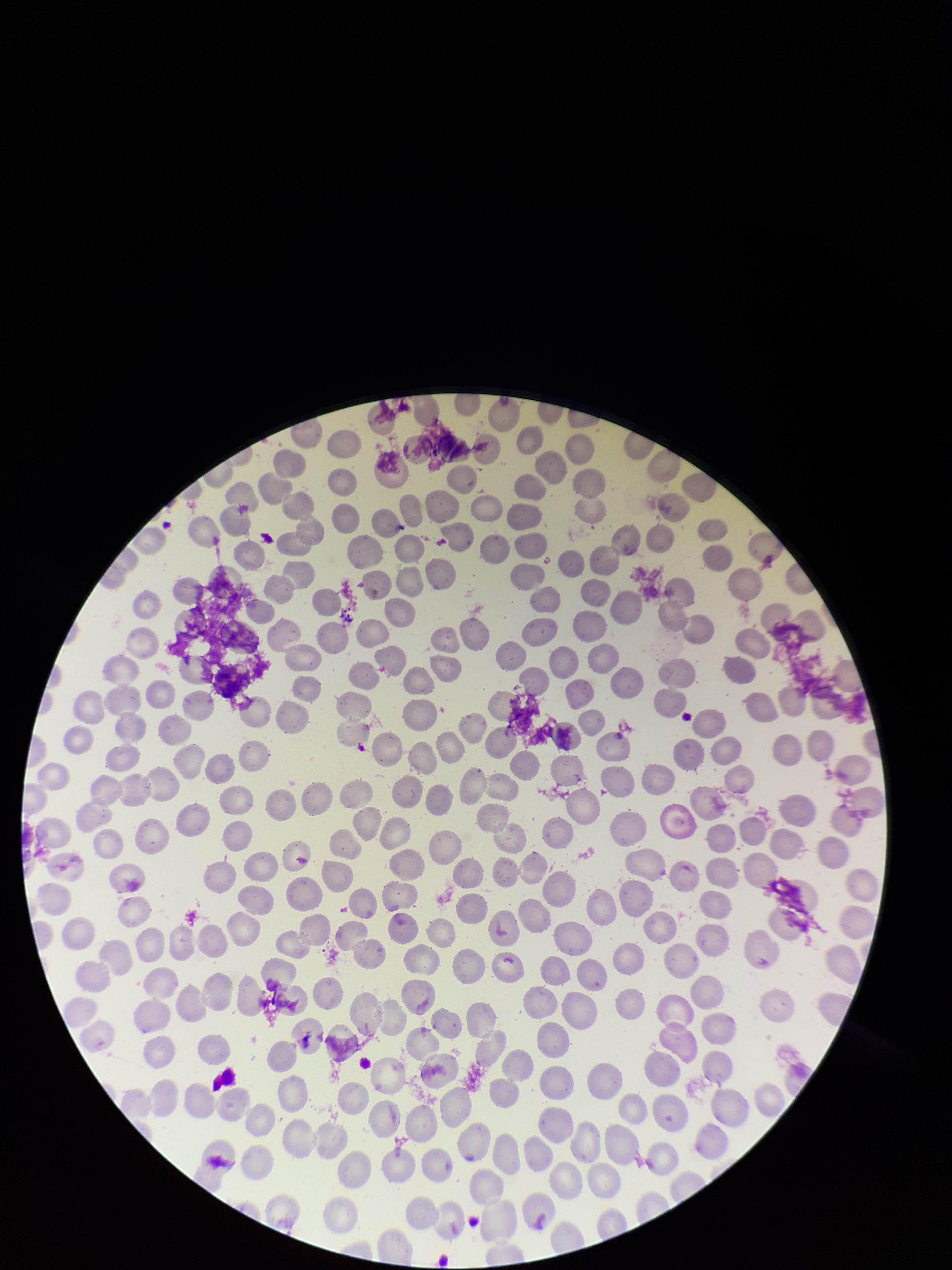 Parasitized red blood cells: none detected. Giemsa stain. Preparation: thin smear. Image is 952×1270 pixels. Red blood cell count: 210. One field from this slide. Parasitized red blood cell count: 0. Patient malaria status: negative. Smartphone photograph taken through the eyepiece of a microscope.